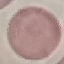

{
  "result": "negative for malaria parasites",
  "stain": "Giemsa",
  "image_type": "cell patch, automatically extracted from a larger field of view and resized to 64 × 64 pixels",
  "capture": "smartphone through the microscope eyepiece",
  "preparation": "thin blood film"
}